Give the extent of all Plasmodium malariae-infected red blood cells.
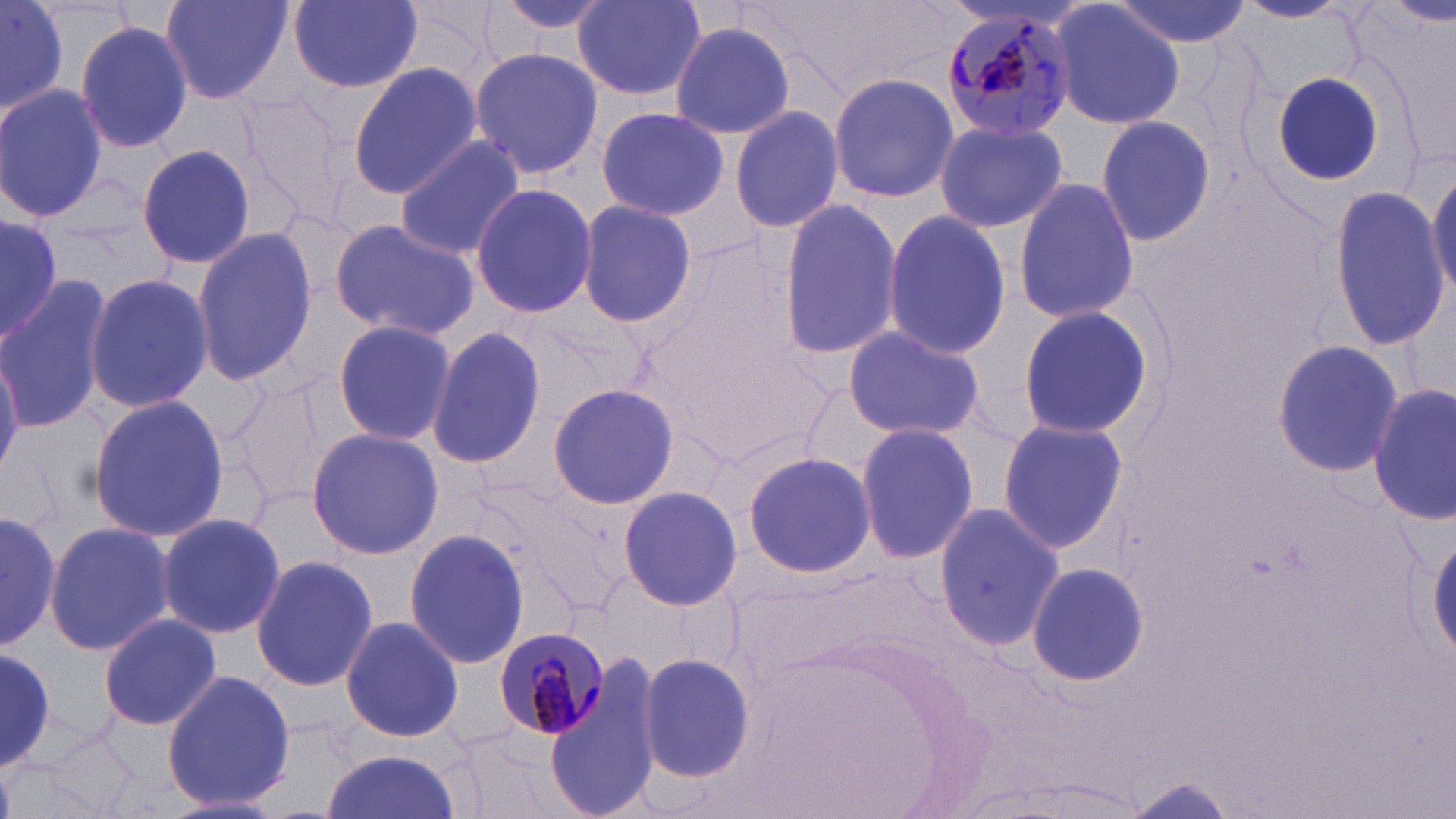

Approximate bounding boxes as (x1, y1, x2, y2) in pixels.
Plasmodium malariae-infected red blood cells: (940, 4, 1076, 139), (493, 623, 611, 739).

slide-level diagnosis = Plasmodium malariae
uninfected red blood cell locations = approximate bounding boxes as (x1, y1, x2, y2) in pixels: (0, 0, 71, 120), (159, 0, 293, 104), (289, 0, 424, 92), (488, 0, 619, 39), (569, 0, 706, 101), (1109, 0, 1251, 47), (1235, 0, 1354, 24), (1388, 0, 1454, 29), (1050, 1, 1184, 132), (74, 20, 192, 156), (669, 20, 797, 138), (470, 46, 601, 180), (348, 62, 482, 199), (1270, 70, 1387, 186), (829, 72, 957, 205), (0, 86, 108, 221), (236, 90, 353, 227), (725, 95, 953, 220), (729, 104, 845, 235), (595, 106, 730, 221), (1093, 113, 1217, 245), (932, 118, 1067, 234), (394, 135, 524, 260), (135, 144, 258, 268), (1428, 163, 1456, 301), (1012, 177, 1139, 323), (470, 183, 597, 319), (1329, 187, 1451, 349), (779, 198, 903, 359), (578, 200, 696, 327), (882, 207, 1013, 360), (0, 214, 59, 345), (329, 219, 480, 340), (189, 227, 319, 387), (83, 272, 213, 411), (0, 282, 109, 430), (1015, 305, 1158, 442), (331, 318, 458, 447), (842, 325, 987, 442), (425, 327, 547, 471), (1270, 340, 1402, 478), (0, 349, 22, 482), (231, 376, 335, 507), (547, 381, 678, 511), (1370, 384, 1454, 529), (84, 392, 232, 545), (995, 416, 1130, 555), (855, 423, 981, 564), (306, 427, 443, 559), (742, 450, 877, 579), (617, 486, 742, 611), (933, 501, 1063, 654), (0, 508, 62, 653), (156, 513, 286, 640), (41, 520, 173, 658), (403, 527, 530, 671), (1428, 527, 1456, 661), (251, 554, 378, 691), (1025, 562, 1149, 685), (97, 612, 222, 731), (339, 613, 466, 743), (0, 644, 57, 776), (636, 651, 756, 784), (545, 660, 665, 819), (160, 669, 296, 813), (34, 726, 147, 819), (447, 726, 579, 819), (318, 750, 464, 819), (1121, 777, 1242, 816)
field of view = single
stain = May-Grünwald-Giemsa
preparation = thin blood film
image size = 1456×819 pixels
magnification = 1000x
modality = light microscopy